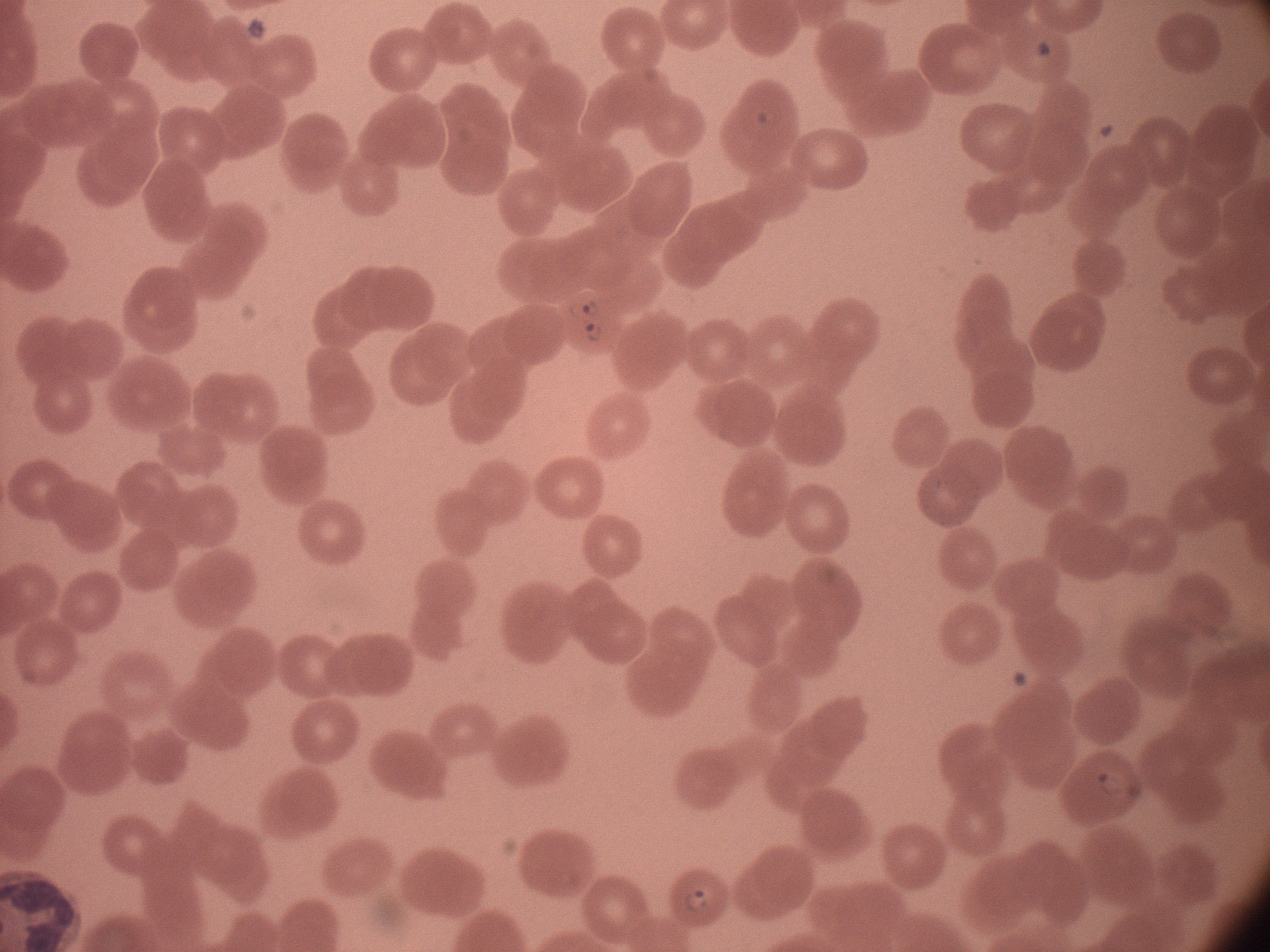 Approximate bounding boxes as named x1/y1/x2/y2 corners in pixels, from the source annotation, which is not necessarily exhaustive. Ring form locations: (x1=743, y1=97, x2=786, y2=139), (x1=565, y1=293, x2=607, y2=326), (x1=578, y1=323, x2=608, y2=349), (x1=1088, y1=763, x2=1134, y2=806), (x1=677, y1=883, x2=714, y2=920). Giemsa-stained preparation. Species: Plasmodium falciparum. Thin blood smear. Leica DM2000 optical microscope with a built-in camera. Single field of view. Captured at 100x magnification. Image is 1270×952 pixels.